Assess the morphology of the erythrocytes.
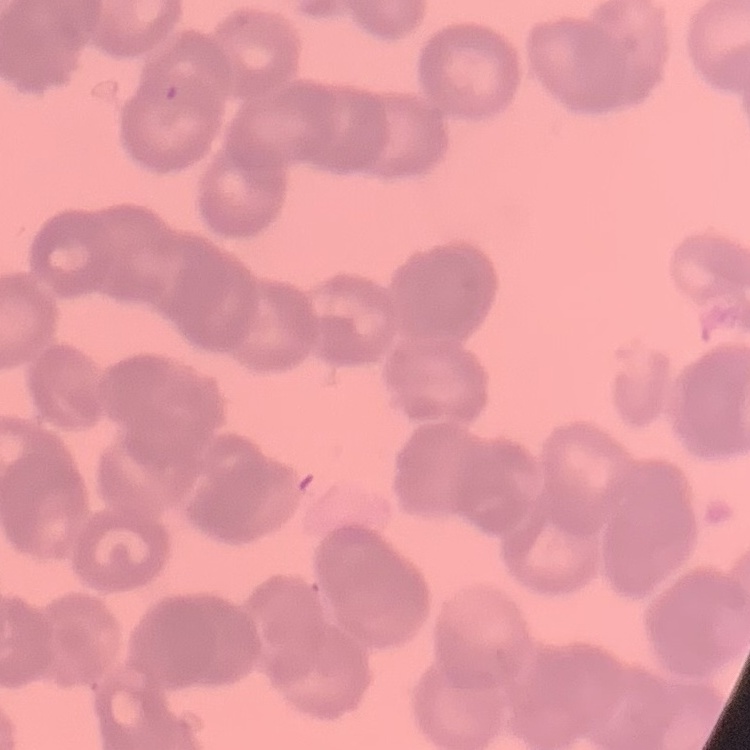

They show rouleaux formation.

Summary:
  - Image type: square crop of a larger photomicrograph
  - Preparation: thin blood smear
  - Stain: Field's or Giemsa